Report the malaria status.
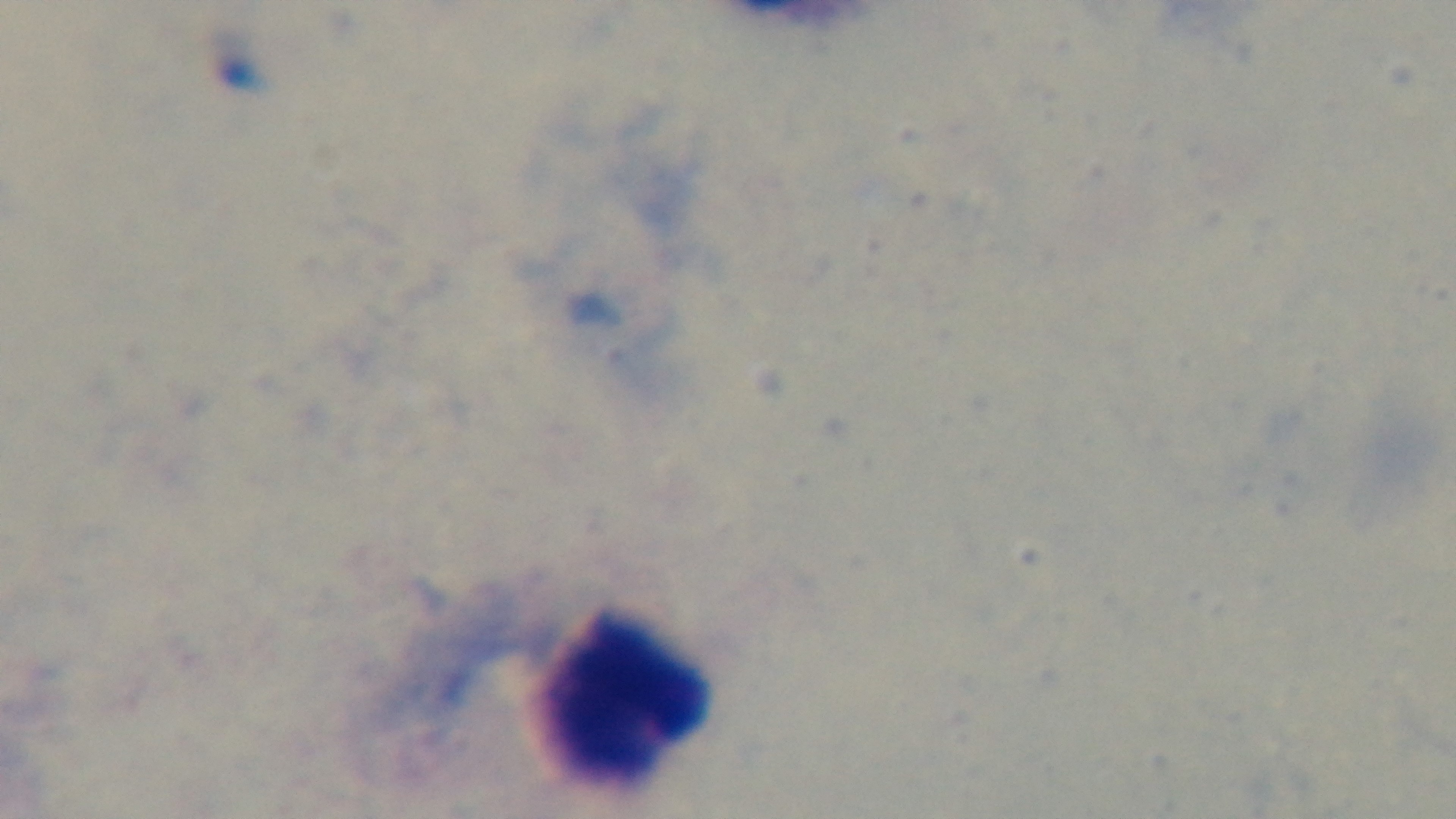
Negative.

field of view = one from the slide
objective = 100x oil immersion
capture = mounted 4K digital camera
preparation = thick blood film
stain = Giemsa
modality = light microscopy